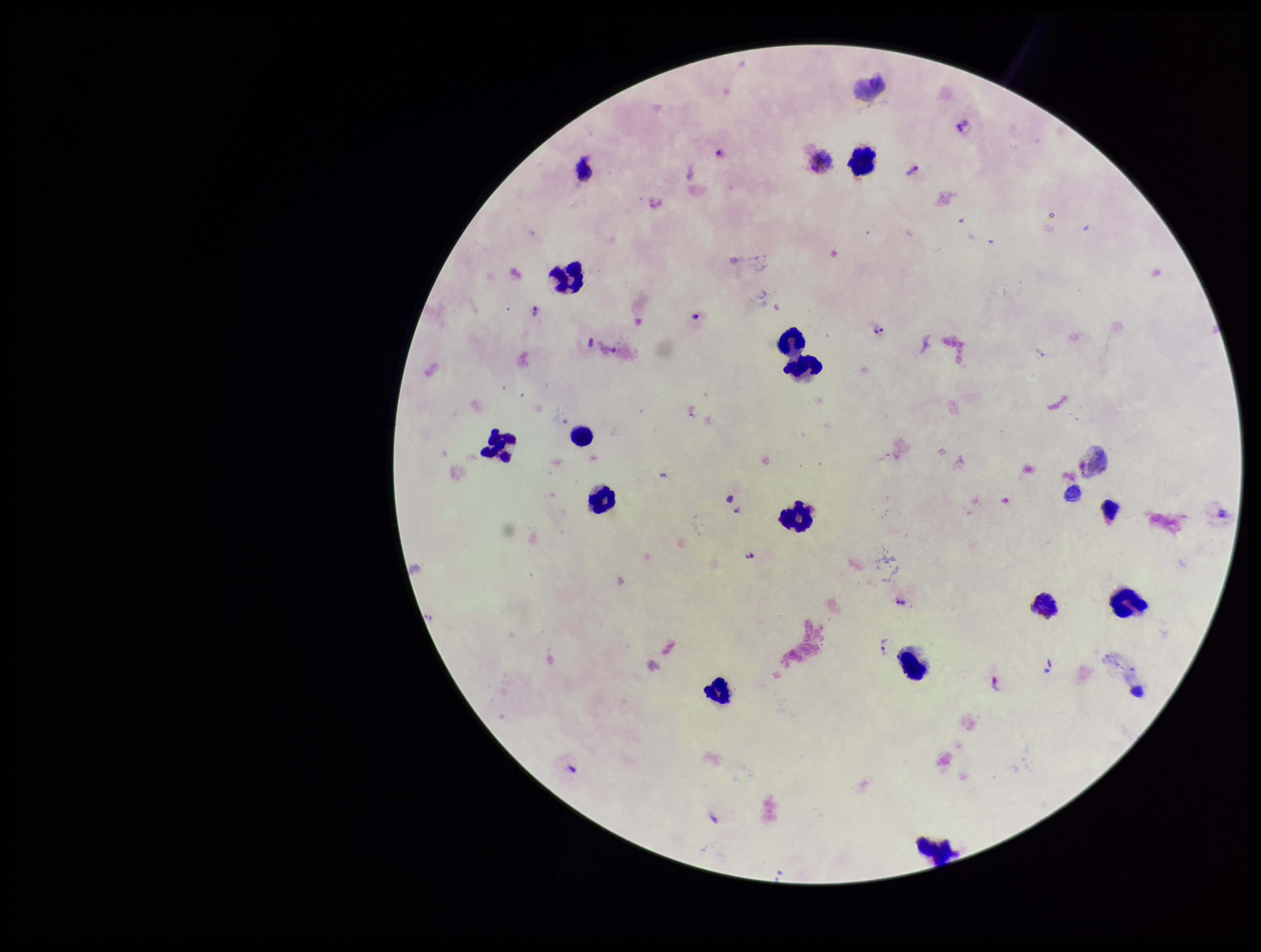

image size = 1261×952 pixels
leukocyte count = 18
Plasmodium parasites = detected
field of view = one from this slide
capture = smartphone photograph through the microscope eyepiece
stain = Giemsa
species reported for this patient = Plasmodium vivax
parasite count = 15
preparation = thick blood smear
patient malaria status = infected